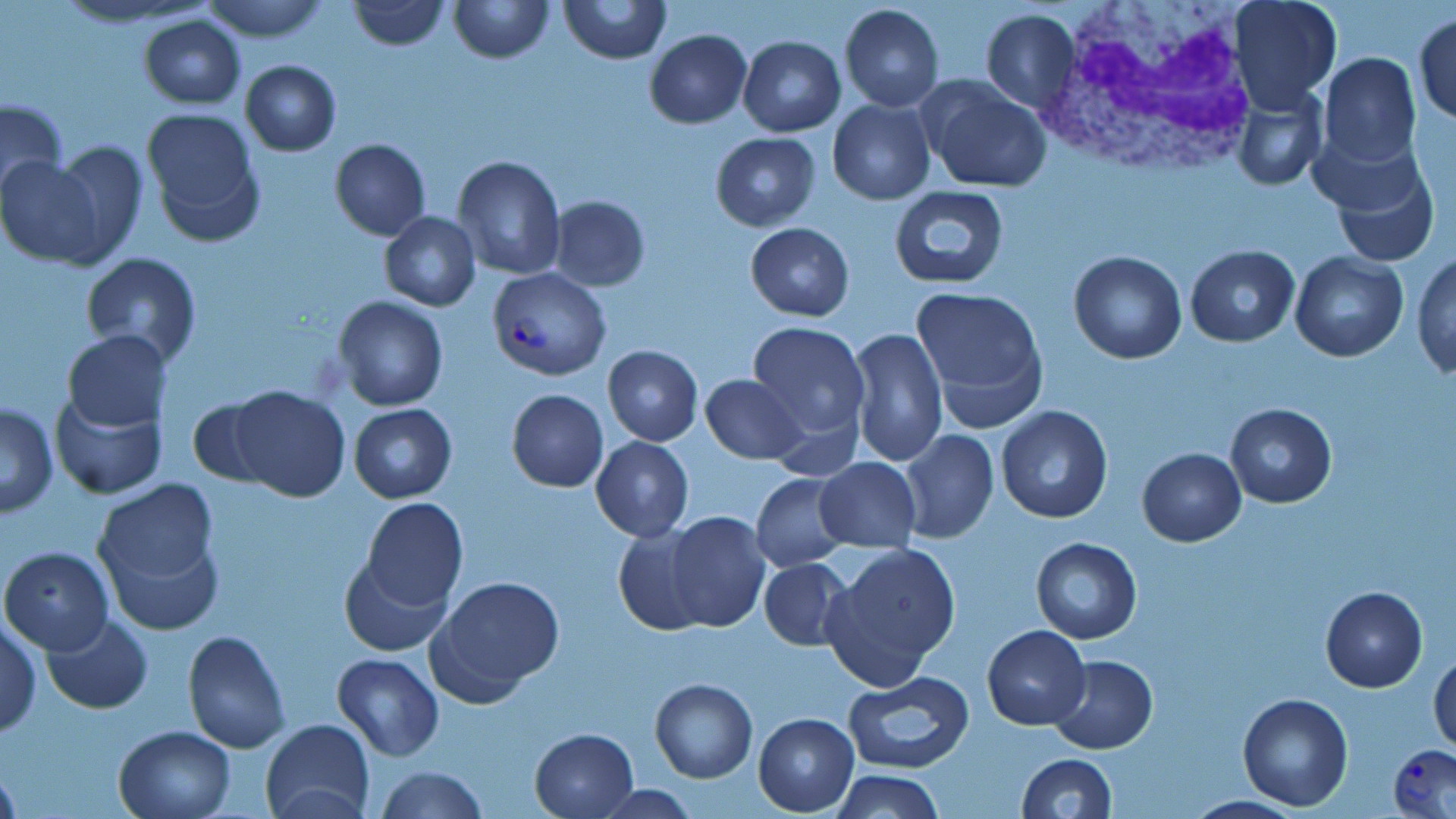
Summary:
  - Coordinate format: approximate bounding boxes as (x1,y1)-(x2,y2) corner pairs in pixels
  - Uninfected red blood cell locations: (348,0)-(449,50), (447,0)-(553,64), (558,0)-(669,66), (1229,0)-(1340,110), (199,1)-(333,44), (839,4)-(944,112), (980,9)-(1079,112), (1414,13)-(1456,126), (138,15)-(245,108), (644,29)-(751,128), (739,36)-(845,137), (1320,53)-(1421,169), (240,60)-(341,155), (919,78)-(1052,193), (1231,89)-(1325,192), (0,97)-(67,206), (827,99)-(934,205), (143,110)-(263,243), (711,132)-(820,231), (48,139)-(147,262), (329,140)-(431,240), (1327,150)-(1440,268), (0,155)-(108,267), (453,155)-(566,281), (888,184)-(1012,291), (547,195)-(651,291), (380,212)-(480,311), (746,223)-(853,321), (1186,245)-(1299,347), (1068,249)-(1187,364), (1411,250)-(1455,379), (1290,251)-(1408,362), (79,254)-(202,369), (911,287)-(1048,422), (335,296)-(449,412), (746,320)-(871,443), (848,326)-(949,471), (62,329)-(172,433), (602,345)-(702,445), (699,373)-(805,465), (224,386)-(351,501), (506,390)-(608,491), (48,391)-(167,500), (188,395)-(279,488), (1,401)-(58,517), (1224,402)-(1336,509), (349,403)-(456,503), (996,405)-(1113,523), (899,429)-(997,542), (590,436)-(693,542), (1136,448)-(1246,546), (815,458)-(921,552), (752,472)-(852,572), (91,478)-(221,597), (360,497)-(468,610), (664,511)-(768,631), (612,527)-(711,636), (1030,538)-(1142,643), (823,543)-(961,688), (1,546)-(114,655), (338,555)-(453,657), (758,558)-(852,650), (433,573)-(567,696), (1320,586)-(1428,693), (1,615)-(41,740), (41,615)-(152,713), (982,625)-(1090,730), (182,630)-(290,754), (1429,648)-(1455,754), (332,653)-(443,760), (1046,655)-(1158,754), (842,670)-(975,775), (650,678)-(757,782), (1237,692)-(1354,812), (754,713)-(857,815), (261,719)-(375,818), (113,725)-(236,818), (529,727)-(639,817), (1016,752)-(1117,818), (0,764)-(19,818), (377,765)-(487,819), (832,769)-(944,819), (591,783)-(703,817)
  - Plasmodium vivax-infected red blood cell locations: (489,268)-(610,381), (1387,744)-(1456,818)
  - White blood cell locations: (1038,0)-(1259,173)
  - Slide-level diagnosis: Plasmodium vivax
  - Field of view: one of a larger specimen
  - Modality: optical microscopy
  - Image size: 1456×819 pixels
  - Magnification: 1000x
  - Preparation: thin blood film
  - Stain: May-Grünwald-Giemsa